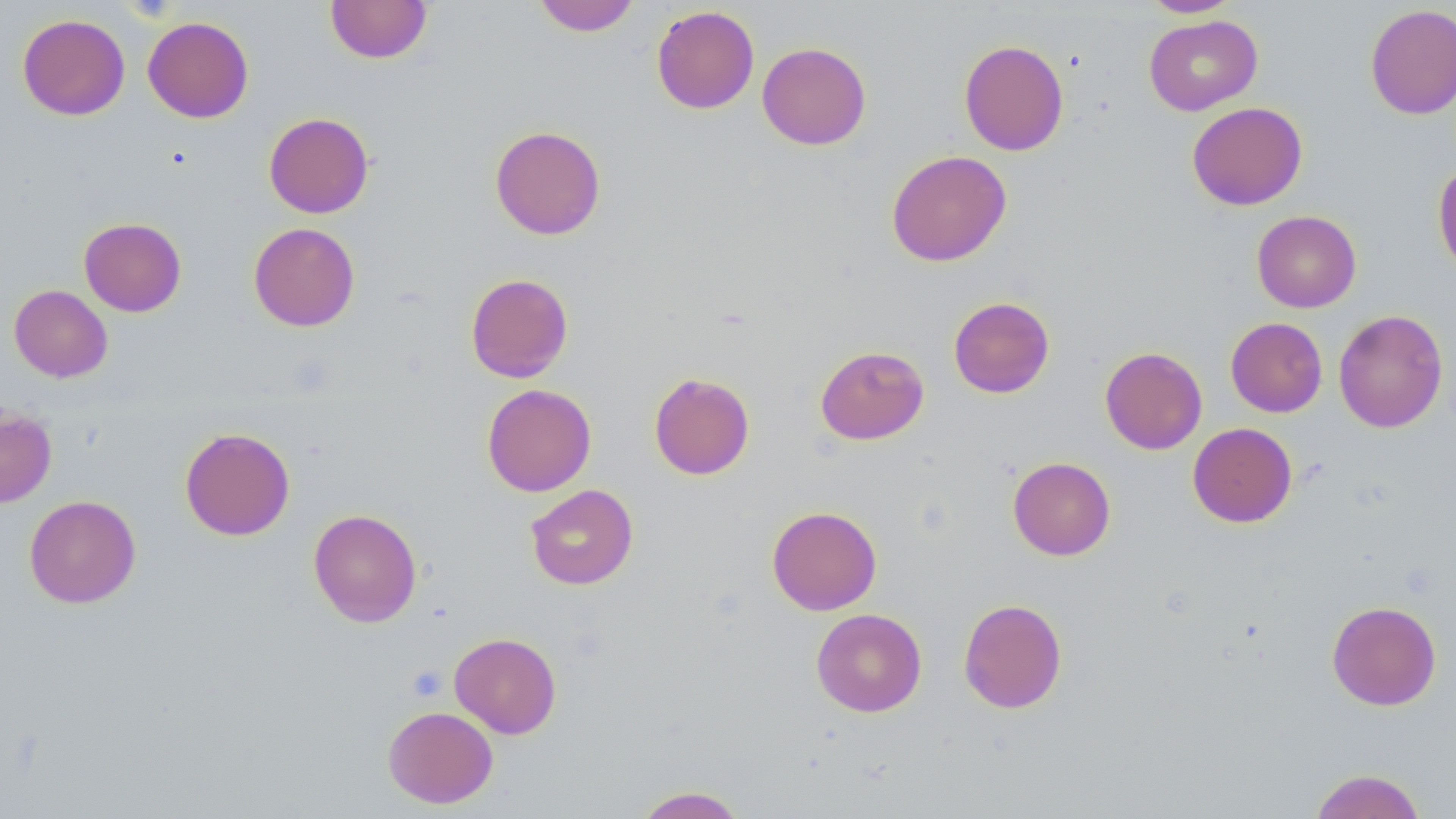
Approximate bounding boxes as (x1, y1, x2, y2) in pixels. Uninfected red blood cell locations: (325, 0, 433, 64), (533, 0, 640, 36), (1140, 0, 1242, 18), (1365, 4, 1456, 120), (651, 5, 760, 114), (17, 14, 130, 120), (1144, 15, 1262, 115), (142, 16, 254, 123), (958, 39, 1069, 156), (757, 42, 872, 150), (1187, 101, 1308, 210), (263, 112, 374, 218), (490, 125, 606, 240), (886, 150, 1011, 267), (1432, 162, 1456, 276), (1251, 210, 1361, 312), (79, 217, 187, 317), (248, 222, 360, 332), (465, 273, 574, 383), (9, 285, 112, 382), (948, 296, 1055, 398), (1333, 309, 1448, 433), (1225, 317, 1327, 417), (815, 345, 929, 445), (1100, 347, 1207, 454), (648, 372, 755, 480), (482, 383, 596, 497), (0, 407, 57, 507), (1187, 422, 1297, 527), (179, 426, 296, 541), (1007, 456, 1116, 561), (525, 484, 638, 590), (24, 494, 141, 608), (766, 505, 882, 615), (308, 508, 422, 627), (958, 598, 1067, 714), (1327, 600, 1441, 710), (811, 608, 927, 717), (449, 632, 562, 739), (383, 705, 498, 808), (1309, 768, 1427, 819), (633, 786, 747, 818). Platelet locations: (406, 664, 447, 702). Slide-level diagnosis: negative for blood parasites. 1000x magnification. May-Grünwald-Giemsa-stained preparation. Thin blood smear. Image is 1456×819 pixels. One field of a larger specimen. Optical microscopy.